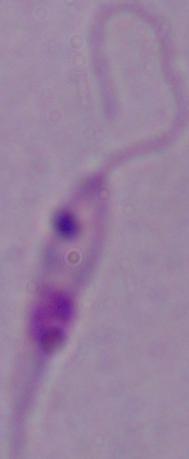

identification: Leishmania
magnification: 1000x
modality: photomicrograph